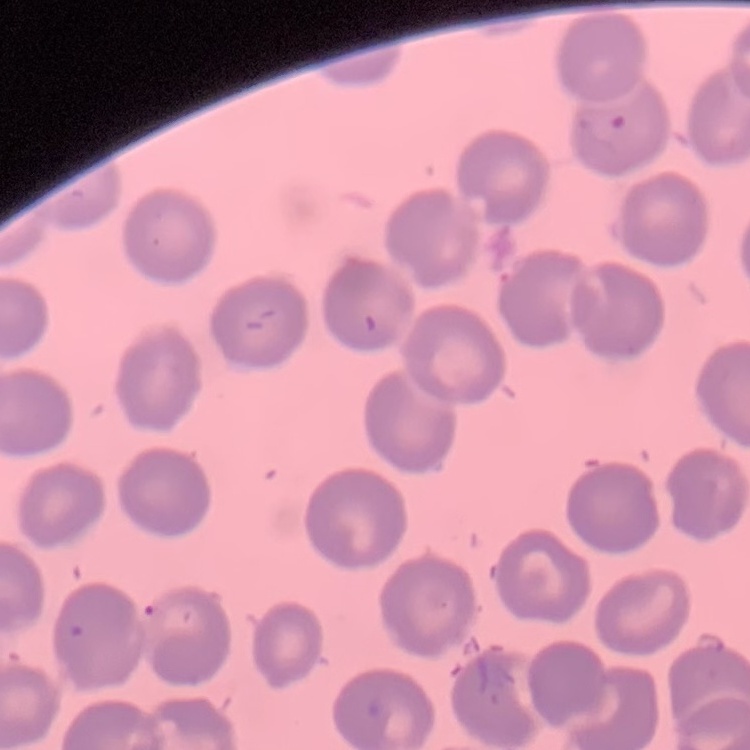

Summary:
  - Erythrocyte morphology: no rouleaux formation
  - Preparation: thin peripheral smear
  - Image type: square crop of a larger photomicrograph
  - Stain: Field's or Giemsa